Outline each Plasmodium malariae-infected red blood cell.
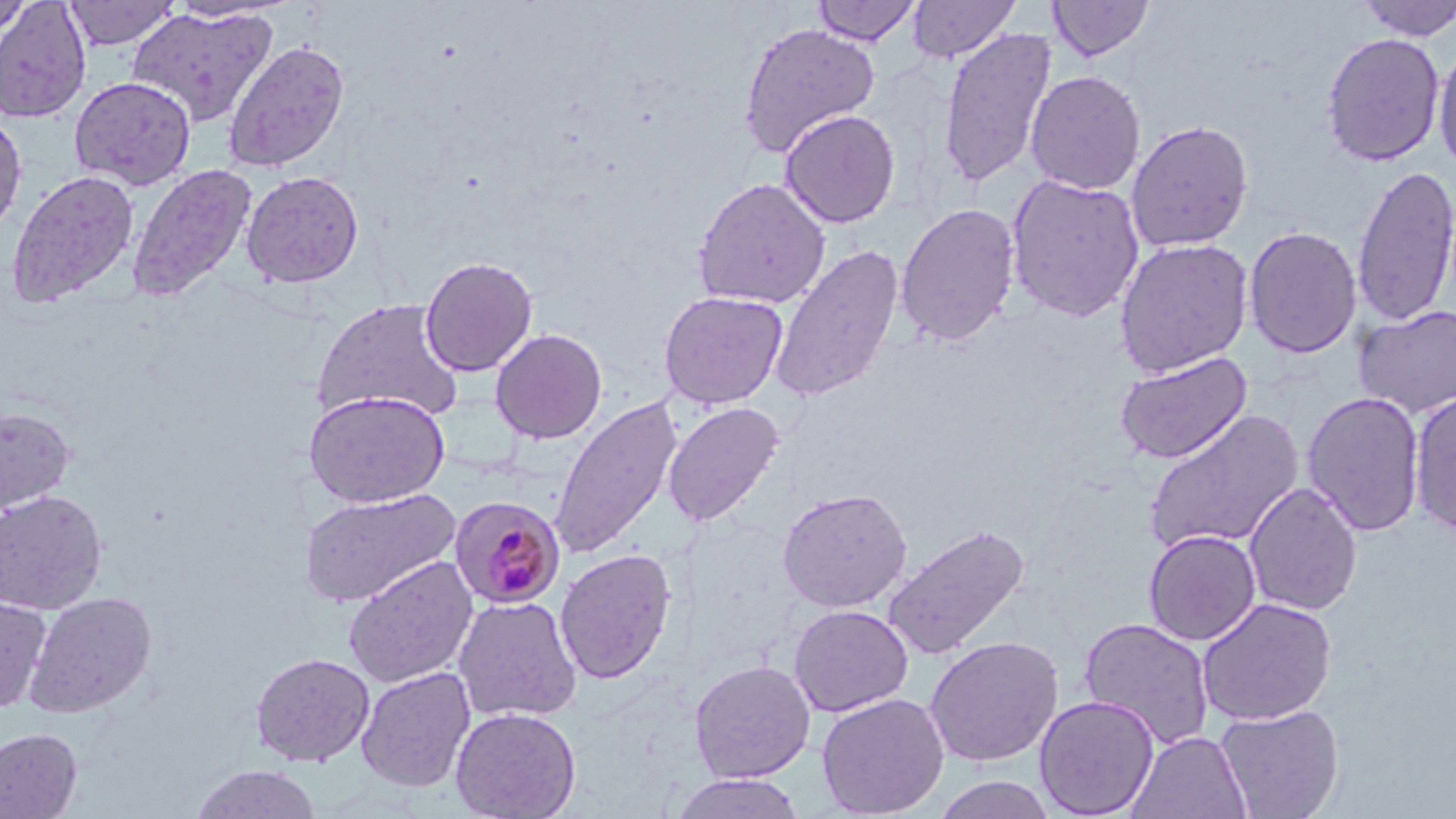
Approximate bounding boxes as [x1, y1, x2, y2] in pixels.
Plasmodium malariae-infected red blood cells: [448, 494, 566, 609].

slide-level diagnosis = Plasmodium malariae
uninfected red blood cell locations = approximate bounding boxes as [x1, y1, x2, y2] in pixels: [0, 0, 34, 37], [63, 0, 180, 49], [811, 0, 922, 46], [907, 0, 1021, 63], [1047, 0, 1155, 61], [1356, 0, 1456, 41], [0, 1, 92, 123], [166, 1, 288, 23], [127, 6, 277, 127], [738, 22, 881, 157], [938, 27, 1057, 188], [1321, 31, 1445, 166], [222, 39, 350, 172], [1432, 42, 1456, 176], [1025, 70, 1146, 195], [69, 76, 196, 190], [779, 109, 901, 228], [0, 111, 27, 236], [1125, 119, 1254, 253], [127, 164, 257, 302], [1352, 164, 1456, 328], [7, 170, 140, 307], [242, 170, 364, 288], [1005, 173, 1145, 323], [693, 177, 831, 309], [895, 202, 1020, 346], [1243, 226, 1362, 359], [1114, 238, 1253, 377], [769, 245, 904, 403], [419, 256, 538, 377], [658, 290, 788, 409], [312, 297, 465, 424], [1354, 304, 1456, 419], [490, 328, 607, 444], [1114, 351, 1253, 464], [304, 390, 451, 507], [1302, 391, 1426, 536], [1410, 391, 1456, 536], [549, 397, 684, 560], [663, 402, 784, 527], [0, 407, 76, 515], [1142, 408, 1305, 556], [1244, 483, 1363, 616], [777, 487, 912, 612], [300, 488, 460, 608], [0, 490, 107, 614], [882, 522, 1031, 662], [1143, 530, 1261, 645], [555, 548, 677, 684], [343, 555, 478, 688], [25, 591, 157, 718], [0, 594, 52, 714], [453, 596, 582, 722], [1197, 598, 1337, 726], [788, 604, 913, 717], [1078, 617, 1215, 749], [925, 636, 1063, 766], [251, 652, 375, 767], [689, 660, 816, 783], [356, 666, 476, 792], [817, 693, 949, 818], [1034, 695, 1159, 818], [1215, 704, 1345, 819], [450, 706, 581, 819], [0, 728, 82, 818], [1126, 730, 1251, 819], [190, 764, 321, 819], [671, 773, 806, 818], [932, 775, 1059, 819]
field of view = one of a larger specimen
image size = 1456×819 pixels
magnification = 1000x
modality = optical microscopy
stain = May-Grünwald-Giemsa
preparation = thin blood smear